Report the malaria status of this cell.
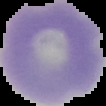
Uninfected.

image type = segmented cell region on a black background
image size = 106×106 pixels
preparation = thin blood smear